Report the malaria status of this cell.
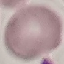

Uninfected.

preparation: thin smear
stain: Giemsa
image_type: cell patch, automatically extracted from a larger field of view and resized to 64 × 64 pixels
capture: smartphone through the microscope eyepiece